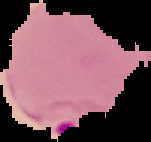

image type = segmented cell region on a black background
preparation = thin blood film
image size = 151×142 pixels
result = malaria parasites identified